Report the malaria status of this cell.
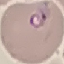
Parasitized.

Summary:
  - Capture: smartphone camera at the microscope eyepiece
  - Preparation: thin blood smear
  - Image type: cell patch, automatically extracted from a larger field of view and resized to 64 × 64 pixels
  - Stain: Giemsa